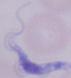 A trypanosome is shown. Captured at 1000x magnification. Micrograph.